Name the parasite shown.
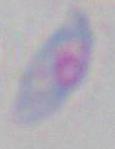

This is Toxoplasma gondii.

{
  "modality": "micrograph",
  "magnification": "1000x"
}